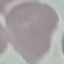 Malaria status: uninfected. Photographed with a smartphone camera at the microscope eyepiece. Thin smear of blood. Giemsa-stained preparation. Automatically extracted cell patch, resized to 64 × 64 pixels.